Outline each blood parasite and name the species.
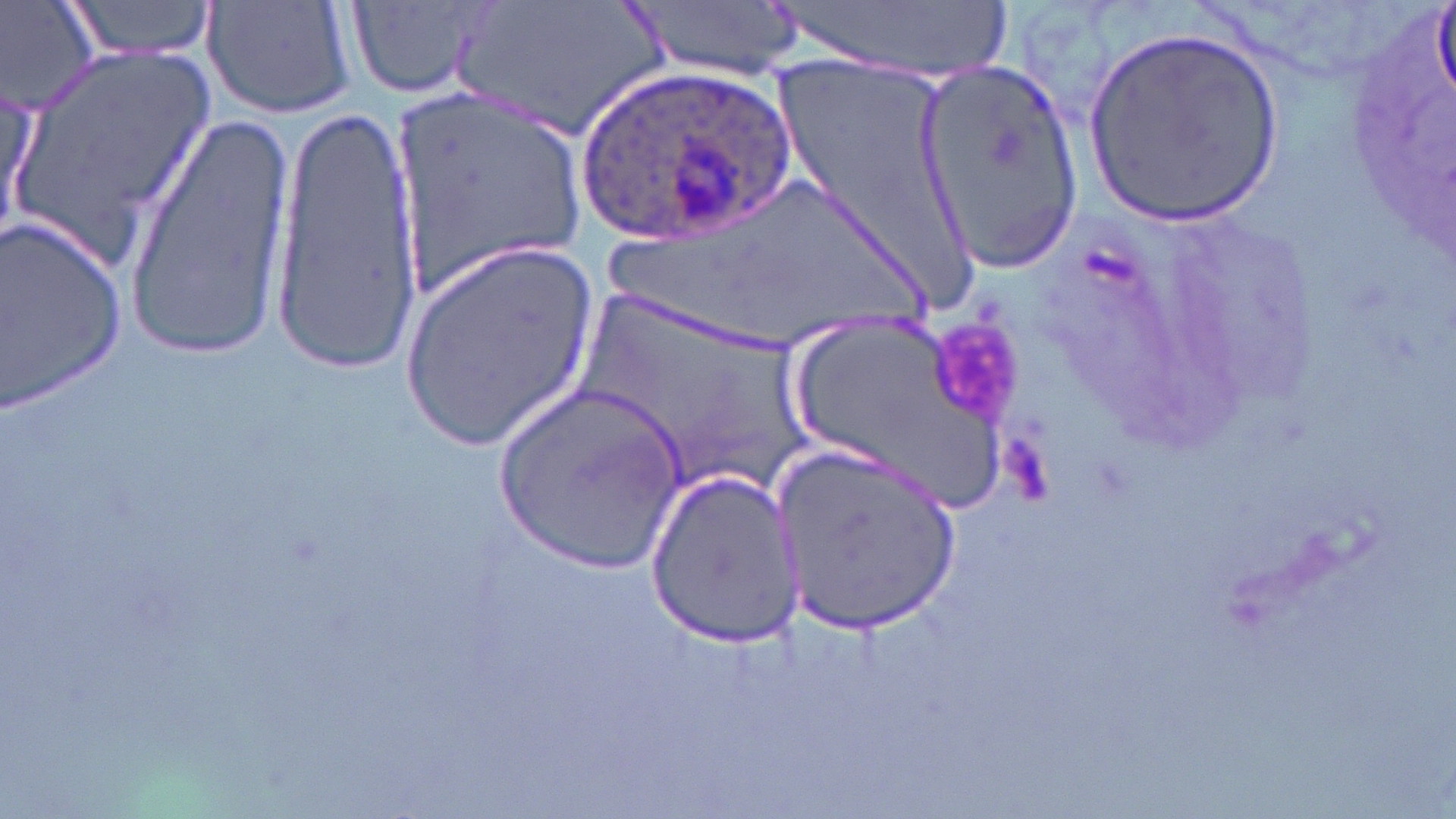

Approximate bounding boxes as named x1/y1/x2/y2 corners in pixels.
Plasmodium ovale-infected red blood cells: (x1=575, y1=69, x2=792, y2=247).
No Plasmodium falciparum, Plasmodium malariae, Plasmodium vivax, Babesia divergens, or Trypanosoma brucei observed.

slide-level diagnosis = Plasmodium ovale
platelet locations = approximate bounding boxes as named x1/y1/x2/y2 corners in pixels: (x1=931, y1=318, x2=1031, y2=428)
stain = May-Grünwald-Giemsa
preparation = thin blood film
field of view = one of a larger specimen
image size = 1456×819 pixels
modality = light microscopy
uninfected red blood cell locations = approximate bounding boxes as named x1/y1/x2/y2 corners in pixels: (x1=1, y1=0, x2=102, y2=114), (x1=57, y1=0, x2=222, y2=65), (x1=203, y1=0, x2=359, y2=121), (x1=448, y1=0, x2=676, y2=143), (x1=629, y1=0, x2=806, y2=83), (x1=764, y1=0, x2=1017, y2=83), (x1=351, y1=1, x2=492, y2=99), (x1=1082, y1=31, x2=1285, y2=228), (x1=10, y1=38, x2=219, y2=263), (x1=916, y1=56, x2=1085, y2=275), (x1=768, y1=57, x2=965, y2=280), (x1=385, y1=80, x2=590, y2=298), (x1=2, y1=92, x2=44, y2=243), (x1=266, y1=95, x2=421, y2=368), (x1=124, y1=111, x2=300, y2=356), (x1=596, y1=180, x2=936, y2=356), (x1=1, y1=212, x2=126, y2=415), (x1=399, y1=244, x2=598, y2=453), (x1=576, y1=283, x2=816, y2=497), (x1=774, y1=309, x2=1026, y2=510), (x1=497, y1=382, x2=689, y2=571), (x1=771, y1=440, x2=962, y2=642), (x1=642, y1=472, x2=804, y2=646)
magnification = 1000x